Assess the morphology of the red blood cells.
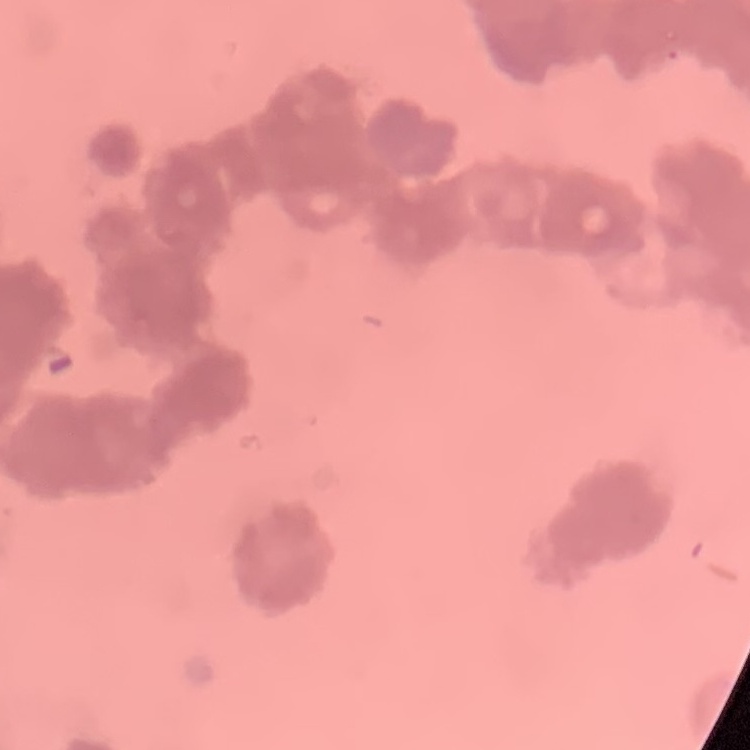
Rouleaux formation.

image type = one tile cut from a larger photomicrograph
stain = Field's or Giemsa
preparation = thin blood smear